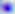
identification = Toxoplasma gondii
magnification = 400x
modality = photomicrograph